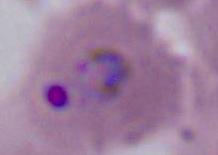
{
  "magnification": "400x or 1000x",
  "identification": "Plasmodium",
  "modality": "photomicrograph"
}